Identify the blood parasite species.
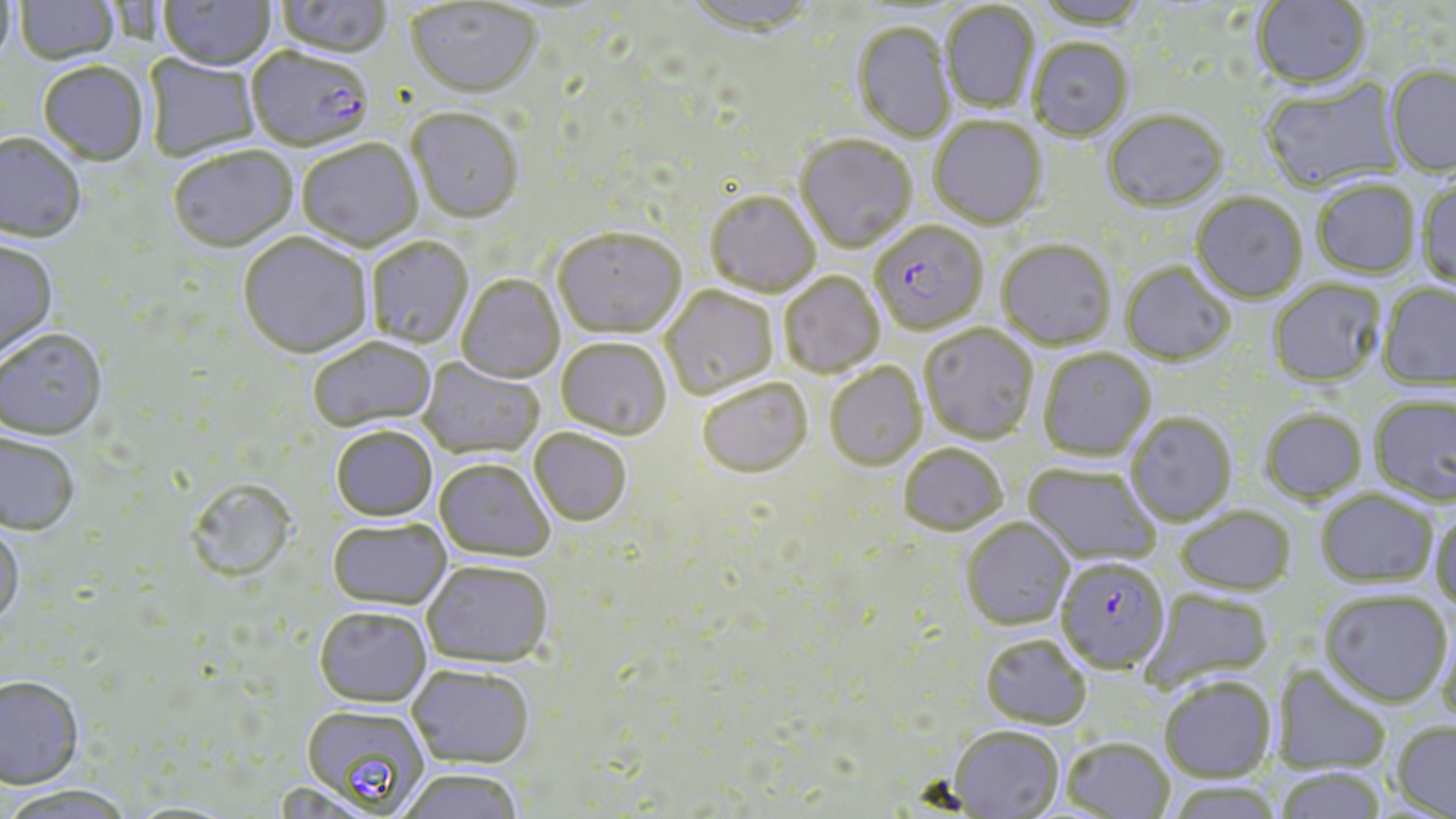
Plasmodium falciparum.

Summary:
  - Coordinate format: approximate bounding boxes as named x1/y1/x2/y2 corners in pixels
  - Plasmodium falciparum-infected red blood cell locations: (x1=246, y1=50, x2=375, y2=153), (x1=870, y1=223, x2=988, y2=336), (x1=1055, y1=557, x2=1171, y2=674)
  - Uninfected red blood cell locations: (x1=159, y1=0, x2=276, y2=74), (x1=273, y1=0, x2=392, y2=61), (x1=683, y1=0, x2=817, y2=42), (x1=1034, y1=0, x2=1148, y2=32), (x1=1252, y1=0, x2=1372, y2=92), (x1=0, y1=1, x2=18, y2=74), (x1=14, y1=1, x2=120, y2=67), (x1=406, y1=2, x2=541, y2=102), (x1=941, y1=3, x2=1039, y2=114), (x1=852, y1=23, x2=955, y2=144), (x1=1028, y1=40, x2=1133, y2=143), (x1=144, y1=54, x2=261, y2=162), (x1=38, y1=64, x2=148, y2=167), (x1=1384, y1=65, x2=1456, y2=178), (x1=1260, y1=78, x2=1404, y2=195), (x1=407, y1=110, x2=523, y2=226), (x1=1103, y1=112, x2=1228, y2=214), (x1=929, y1=118, x2=1048, y2=231), (x1=0, y1=135, x2=86, y2=245), (x1=795, y1=136, x2=917, y2=255), (x1=297, y1=141, x2=423, y2=254), (x1=168, y1=148, x2=299, y2=255), (x1=1312, y1=180, x2=1421, y2=279), (x1=1417, y1=182, x2=1456, y2=290), (x1=705, y1=192, x2=820, y2=299), (x1=1191, y1=194, x2=1308, y2=305), (x1=552, y1=231, x2=686, y2=342), (x1=238, y1=234, x2=372, y2=360), (x1=367, y1=238, x2=474, y2=350), (x1=997, y1=241, x2=1116, y2=352), (x1=0, y1=242, x2=59, y2=361), (x1=1120, y1=263, x2=1235, y2=366), (x1=779, y1=274, x2=885, y2=379), (x1=457, y1=276, x2=565, y2=384), (x1=1267, y1=279, x2=1386, y2=388), (x1=1377, y1=284, x2=1456, y2=391), (x1=660, y1=287, x2=779, y2=402), (x1=920, y1=325, x2=1039, y2=445), (x1=0, y1=331, x2=108, y2=443), (x1=308, y1=338, x2=437, y2=434), (x1=556, y1=340, x2=672, y2=442), (x1=1039, y1=348, x2=1157, y2=461), (x1=418, y1=358, x2=545, y2=460), (x1=825, y1=365, x2=927, y2=472), (x1=698, y1=379, x2=813, y2=481), (x1=1369, y1=395, x2=1456, y2=506), (x1=1259, y1=409, x2=1367, y2=504), (x1=1125, y1=413, x2=1237, y2=526), (x1=331, y1=429, x2=437, y2=524), (x1=528, y1=430, x2=631, y2=528), (x1=0, y1=434, x2=79, y2=538), (x1=898, y1=445, x2=1008, y2=536), (x1=434, y1=461, x2=553, y2=565), (x1=1024, y1=463, x2=1163, y2=566), (x1=185, y1=481, x2=298, y2=585), (x1=1316, y1=489, x2=1439, y2=587), (x1=1175, y1=507, x2=1295, y2=595), (x1=1430, y1=509, x2=1456, y2=615), (x1=961, y1=517, x2=1074, y2=631), (x1=327, y1=520, x2=451, y2=612), (x1=0, y1=522, x2=25, y2=632), (x1=422, y1=562, x2=553, y2=669), (x1=1142, y1=589, x2=1275, y2=691), (x1=1320, y1=590, x2=1452, y2=707), (x1=314, y1=610, x2=431, y2=710), (x1=1437, y1=617, x2=1456, y2=729), (x1=979, y1=635, x2=1091, y2=730), (x1=1272, y1=664, x2=1392, y2=775), (x1=407, y1=667, x2=534, y2=770), (x1=1159, y1=676, x2=1277, y2=782), (x1=0, y1=680, x2=84, y2=792), (x1=300, y1=705, x2=429, y2=814), (x1=1392, y1=721, x2=1456, y2=818), (x1=949, y1=726, x2=1064, y2=818), (x1=1062, y1=737, x2=1175, y2=819), (x1=1273, y1=767, x2=1387, y2=819), (x1=397, y1=771, x2=524, y2=819), (x1=1165, y1=781, x2=1284, y2=818), (x1=0, y1=787, x2=136, y2=819)
  - Magnification: 1000x
  - Preparation: thin blood film
  - Stain: May-Grünwald-Giemsa
  - Modality: light microscopy
  - Image size: 1456×819 pixels
  - Field of view: one of a larger specimen